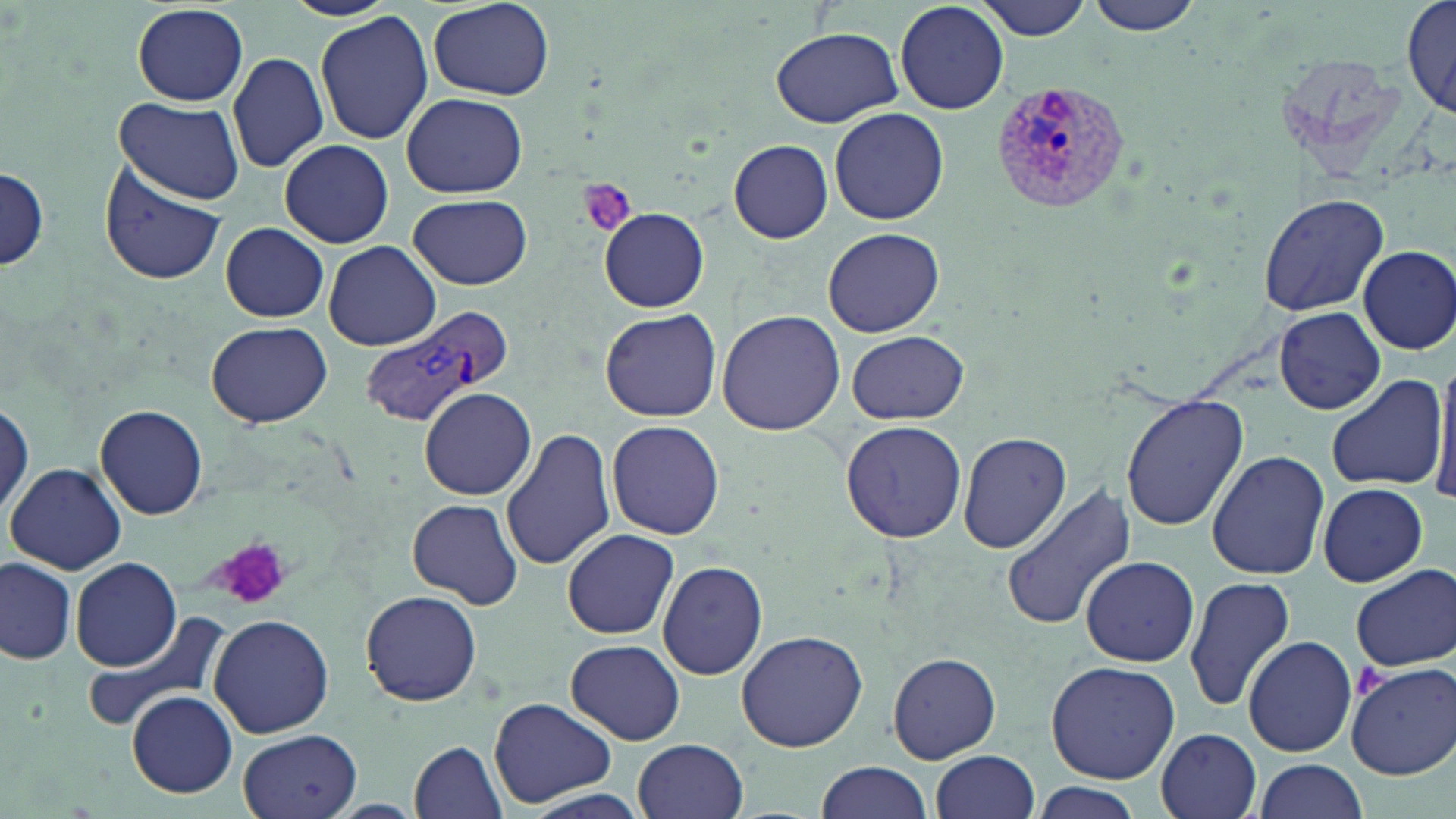

Summary:
  - Coordinate format: approximate bounding boxes as (x1,y1)-(x2,y2) corner pairs in pixels
  - Platelet locations: (577,179)-(639,237), (210,536)-(300,610), (1354,662)-(1386,698)
  - Plasmodium vivax-infected red blood cell locations: (985,77)-(1136,215), (361,312)-(508,427)
  - Uninfected red blood cell locations: (973,0)-(1095,40), (1087,0)-(1203,36), (427,1)-(554,100), (895,1)-(1009,115), (1400,1)-(1455,115), (130,3)-(252,105), (314,11)-(434,144), (770,25)-(903,126), (225,35)-(430,162), (227,52)-(330,174), (402,92)-(528,198), (113,97)-(248,205), (829,106)-(949,225), (278,139)-(394,248), (729,140)-(833,242), (98,159)-(227,287), (0,164)-(50,274), (1259,193)-(1389,318), (408,195)-(533,289), (598,207)-(709,311), (221,222)-(330,322), (821,227)-(945,337), (324,241)-(441,350), (1357,245)-(1456,354), (600,308)-(720,421), (1276,308)-(1385,414), (717,311)-(843,435), (206,321)-(332,427), (846,330)-(970,424), (1431,358)-(1456,508), (1325,373)-(1449,491), (419,388)-(536,500), (1122,394)-(1247,531), (0,397)-(32,521), (95,403)-(208,521), (604,420)-(725,539), (840,421)-(967,542), (500,427)-(616,571), (958,432)-(1070,554), (1206,450)-(1329,580), (5,462)-(127,575), (1000,482)-(1136,629), (1316,483)-(1429,585), (407,498)-(523,609), (562,527)-(679,640), (1079,556)-(1199,667), (0,557)-(77,665), (70,557)-(183,672), (658,561)-(769,681), (1350,564)-(1456,672), (1184,573)-(1297,711), (360,590)-(483,707), (79,612)-(229,737), (208,613)-(332,738), (735,629)-(868,754), (1242,635)-(1358,758), (566,639)-(685,745), (887,650)-(1002,764), (1046,660)-(1181,785), (1347,662)-(1456,778), (127,690)-(238,797), (489,698)-(619,809), (1154,727)-(1262,819), (237,729)-(362,819), (634,738)-(748,819), (408,740)-(509,818), (931,750)-(1040,819), (1251,758)-(1368,819), (814,760)-(935,819), (1030,785)-(1140,819), (513,788)-(656,819)
  - Slide-level diagnosis: Plasmodium vivax
  - Preparation: thin blood film
  - Stain: May-Grünwald-Giemsa
  - Magnification: 1000x
  - Modality: optical microscopy
  - Image size: 1456×819 pixels
  - Field of view: one of a larger specimen